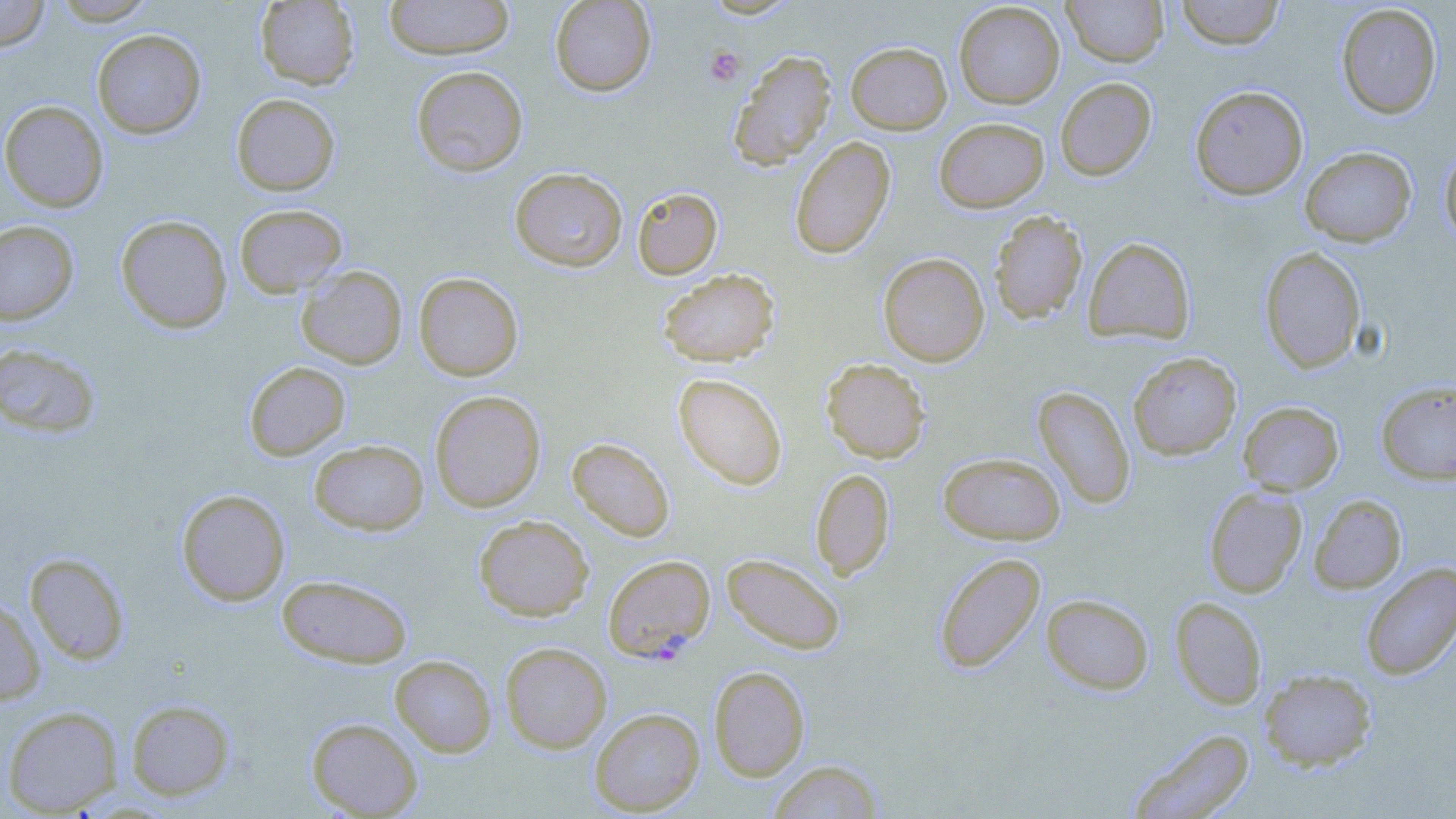

Summary:
  - Coordinate format: approximate bounding boxes as named x1/y1/x2/y2 corners in pixels
  - Platelet locations: (x1=704, y1=46, x2=745, y2=86)
  - Plasmodium falciparum-infected red blood cell locations: (x1=602, y1=553, x2=715, y2=662)
  - Uninfected red blood cell locations: (x1=0, y1=0, x2=50, y2=51), (x1=49, y1=0, x2=159, y2=25), (x1=254, y1=0, x2=360, y2=90), (x1=384, y1=0, x2=515, y2=60), (x1=550, y1=0, x2=656, y2=97), (x1=1174, y1=0, x2=1286, y2=50), (x1=1063, y1=1, x2=1167, y2=66), (x1=953, y1=2, x2=1065, y2=108), (x1=1335, y1=3, x2=1442, y2=119), (x1=92, y1=29, x2=206, y2=139), (x1=846, y1=41, x2=951, y2=134), (x1=728, y1=50, x2=836, y2=171), (x1=410, y1=65, x2=528, y2=177), (x1=1055, y1=77, x2=1156, y2=181), (x1=1190, y1=85, x2=1309, y2=200), (x1=231, y1=94, x2=340, y2=196), (x1=0, y1=100, x2=108, y2=212), (x1=934, y1=117, x2=1049, y2=213), (x1=789, y1=136, x2=895, y2=259), (x1=1439, y1=145, x2=1456, y2=247), (x1=1300, y1=146, x2=1417, y2=247), (x1=509, y1=167, x2=627, y2=272), (x1=632, y1=187, x2=723, y2=279), (x1=234, y1=203, x2=348, y2=298), (x1=989, y1=210, x2=1087, y2=324), (x1=115, y1=214, x2=232, y2=334), (x1=0, y1=219, x2=79, y2=325), (x1=1083, y1=237, x2=1195, y2=345), (x1=1259, y1=247, x2=1366, y2=374), (x1=878, y1=252, x2=989, y2=366), (x1=296, y1=266, x2=407, y2=370), (x1=658, y1=268, x2=779, y2=366), (x1=414, y1=272, x2=523, y2=381), (x1=0, y1=342, x2=102, y2=438), (x1=1128, y1=352, x2=1242, y2=460), (x1=821, y1=358, x2=930, y2=464), (x1=243, y1=361, x2=350, y2=461), (x1=673, y1=373, x2=787, y2=490), (x1=1375, y1=380, x2=1456, y2=484), (x1=1033, y1=386, x2=1135, y2=509), (x1=429, y1=390, x2=545, y2=513), (x1=1238, y1=401, x2=1344, y2=495), (x1=567, y1=437, x2=675, y2=542), (x1=309, y1=439, x2=429, y2=535), (x1=938, y1=452, x2=1065, y2=545), (x1=811, y1=468, x2=895, y2=580), (x1=1204, y1=487, x2=1307, y2=598), (x1=176, y1=489, x2=290, y2=606), (x1=1308, y1=494, x2=1407, y2=594), (x1=474, y1=515, x2=594, y2=621), (x1=25, y1=552, x2=130, y2=665), (x1=933, y1=552, x2=1046, y2=674), (x1=721, y1=553, x2=845, y2=655), (x1=1360, y1=562, x2=1456, y2=681), (x1=275, y1=574, x2=413, y2=668), (x1=1041, y1=594, x2=1154, y2=695), (x1=0, y1=595, x2=46, y2=705), (x1=1170, y1=596, x2=1267, y2=709), (x1=500, y1=642, x2=612, y2=753), (x1=390, y1=655, x2=496, y2=757), (x1=708, y1=665, x2=810, y2=781), (x1=1258, y1=668, x2=1377, y2=771), (x1=126, y1=699, x2=235, y2=801), (x1=2, y1=705, x2=123, y2=816), (x1=589, y1=707, x2=705, y2=815), (x1=306, y1=717, x2=423, y2=818), (x1=1126, y1=727, x2=1255, y2=818), (x1=767, y1=759, x2=885, y2=819)
  - Slide-level diagnosis: Plasmodium falciparum
  - Field of view: one of a larger specimen
  - Magnification: 1000x
  - Preparation: thin blood smear
  - Modality: optical microscopy
  - Image size: 1456×819 pixels
  - Stain: May-Grünwald-Giemsa